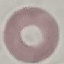

Malaria status: uninfected. Giemsa stain. Thin smear of blood. Acquired by smartphone through the microscope eyepiece. Cell patch, automatically extracted from a larger field of view and resized to 64 × 64 pixels.